Classify this cell by malaria status.
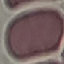

Uninfected.

image type = automatically extracted cell patch, resized to 64 × 64 pixels
stain = Giemsa
preparation = thin blood film
capture = smartphone through the microscope eyepiece